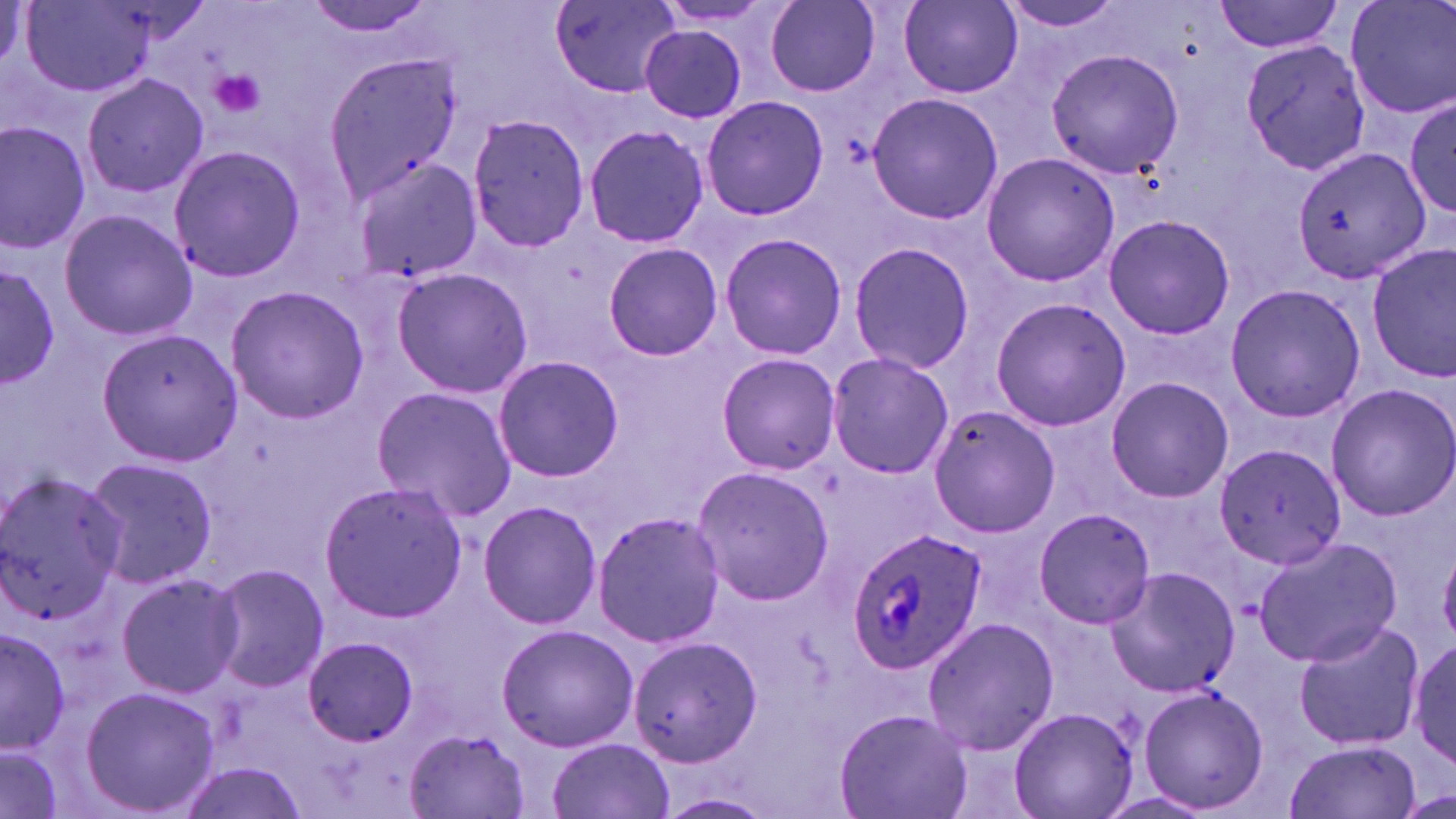
Approximate bounding boxes as named x1/y1/x2/y2 corners in pixels. Platelet locations: (x1=205, y1=70, x2=266, y2=119). Uninfected red blood cell locations: (x1=0, y1=0, x2=33, y2=88), (x1=303, y1=0, x2=443, y2=40), (x1=548, y1=0, x2=685, y2=100), (x1=766, y1=0, x2=882, y2=95), (x1=900, y1=0, x2=1023, y2=96), (x1=998, y1=0, x2=1131, y2=36), (x1=1347, y1=0, x2=1455, y2=120), (x1=21, y1=1, x2=156, y2=96), (x1=1215, y1=1, x2=1347, y2=53), (x1=649, y1=2, x2=786, y2=30), (x1=640, y1=24, x2=749, y2=125), (x1=1241, y1=39, x2=1383, y2=174), (x1=1047, y1=47, x2=1181, y2=180), (x1=322, y1=54, x2=463, y2=200), (x1=82, y1=70, x2=209, y2=198), (x1=867, y1=93, x2=1004, y2=223), (x1=1406, y1=96, x2=1455, y2=218), (x1=698, y1=97, x2=829, y2=221), (x1=468, y1=114, x2=590, y2=255), (x1=0, y1=123, x2=90, y2=254), (x1=582, y1=124, x2=709, y2=248), (x1=165, y1=142, x2=305, y2=285), (x1=1292, y1=145, x2=1431, y2=287), (x1=979, y1=150, x2=1122, y2=288), (x1=350, y1=156, x2=482, y2=283), (x1=58, y1=207, x2=197, y2=343), (x1=1102, y1=213, x2=1237, y2=341), (x1=718, y1=232, x2=847, y2=360), (x1=602, y1=240, x2=724, y2=361), (x1=847, y1=240, x2=976, y2=373), (x1=1367, y1=244, x2=1456, y2=381), (x1=0, y1=260, x2=63, y2=391), (x1=391, y1=268, x2=533, y2=400), (x1=1225, y1=282, x2=1365, y2=422), (x1=224, y1=284, x2=370, y2=424), (x1=989, y1=297, x2=1132, y2=432), (x1=99, y1=328, x2=240, y2=466), (x1=826, y1=351, x2=954, y2=481), (x1=491, y1=353, x2=625, y2=484), (x1=717, y1=353, x2=841, y2=474), (x1=1105, y1=377, x2=1234, y2=503), (x1=1324, y1=383, x2=1456, y2=521), (x1=370, y1=386, x2=518, y2=522), (x1=925, y1=403, x2=1061, y2=538), (x1=1214, y1=443, x2=1347, y2=573), (x1=79, y1=455, x2=221, y2=588), (x1=691, y1=463, x2=836, y2=606), (x1=0, y1=472, x2=125, y2=626), (x1=317, y1=482, x2=469, y2=621), (x1=478, y1=500, x2=602, y2=631), (x1=1030, y1=506, x2=1159, y2=629), (x1=592, y1=512, x2=727, y2=649), (x1=1253, y1=535, x2=1402, y2=667), (x1=211, y1=564, x2=330, y2=691), (x1=1105, y1=568, x2=1241, y2=697), (x1=114, y1=570, x2=245, y2=700), (x1=921, y1=616, x2=1061, y2=755), (x1=1291, y1=618, x2=1424, y2=754), (x1=496, y1=623, x2=638, y2=753), (x1=0, y1=625, x2=71, y2=757), (x1=304, y1=634, x2=421, y2=744), (x1=626, y1=635, x2=762, y2=771), (x1=1407, y1=637, x2=1456, y2=770), (x1=1135, y1=683, x2=1270, y2=814), (x1=78, y1=684, x2=222, y2=818), (x1=1010, y1=703, x2=1139, y2=818), (x1=835, y1=708, x2=972, y2=819), (x1=403, y1=727, x2=532, y2=817), (x1=547, y1=736, x2=674, y2=819), (x1=1285, y1=740, x2=1422, y2=818), (x1=2, y1=745, x2=64, y2=819), (x1=175, y1=757, x2=307, y2=819), (x1=654, y1=792, x2=777, y2=819). Plasmodium ovale-infected red blood cell locations: (x1=848, y1=527, x2=986, y2=675). Slide-level diagnosis: Plasmodium ovale. Image is 1456×819 pixels. May-Grünwald-Giemsa-stained preparation. One field of a larger specimen. 1000x magnification. Thin blood smear. Light microscopy.